Give the position of every Plasmodium parasite.
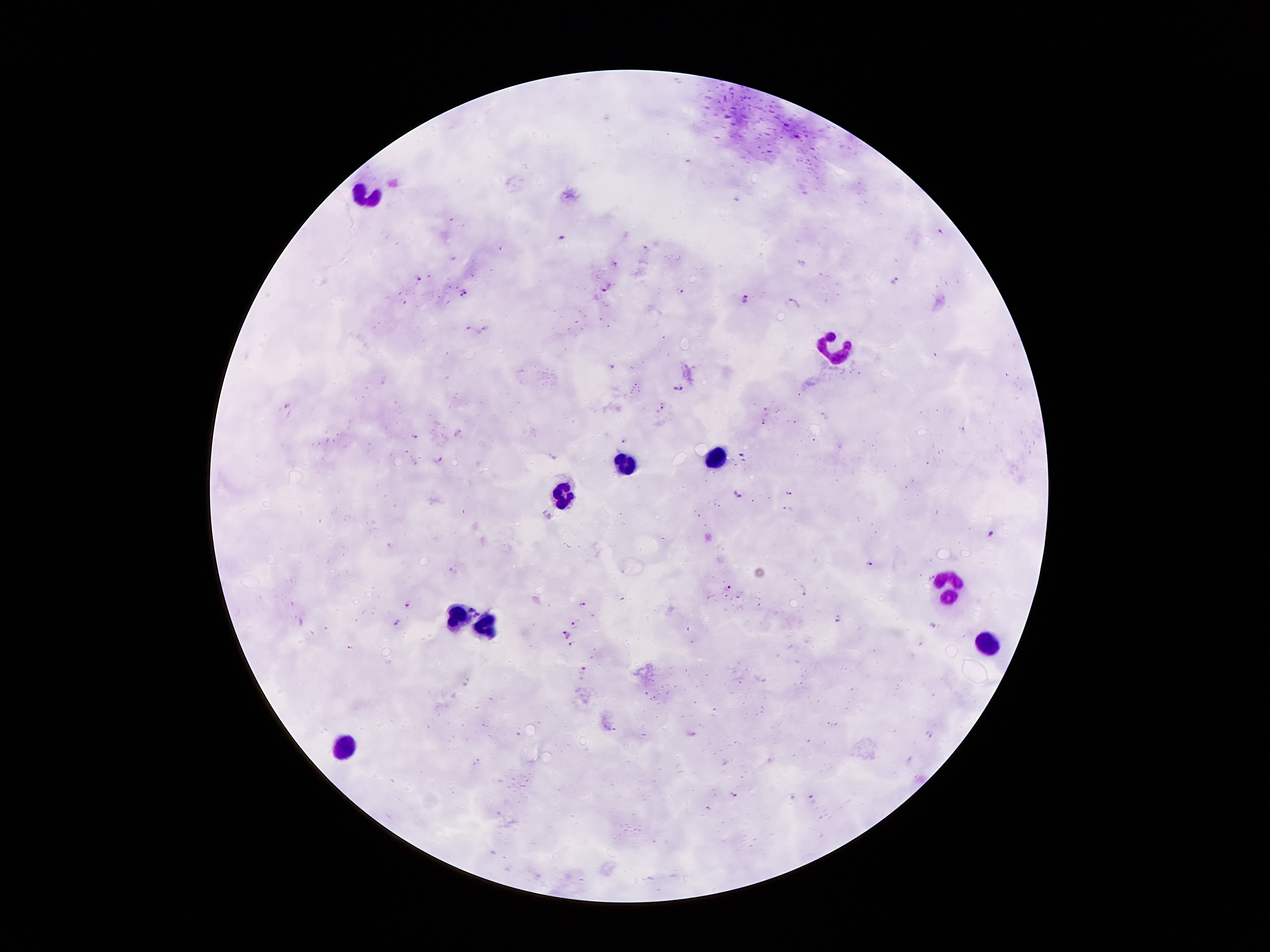
Approximate centers as [x, y] in pixels.
Plasmodium parasites: [940, 232], [562, 237], [615, 262], [419, 278], [897, 282], [609, 288], [465, 292], [680, 292], [747, 297], [794, 302], [484, 330], [613, 365], [678, 388], [288, 404], [662, 407], [793, 421], [762, 422], [962, 429], [458, 433], [414, 438], [624, 439], [439, 459], [790, 493], [738, 495], [992, 533], [870, 563], [453, 570], [729, 588], [804, 592], [582, 603], [408, 605], [837, 618], [399, 622], [575, 625], [933, 625], [566, 635], [571, 643], [584, 668], [930, 734], [735, 793], [812, 799].

Summary:
  - Leukocyte locations: [363, 192], [832, 346], [715, 458], [626, 462], [562, 494], [949, 588], [458, 616], [488, 628], [987, 642], [345, 744]
  - Field of view: single
  - Stain: Giemsa
  - Magnification: 100x
  - Image size: 1270×952 pixels
  - Patient malaria status: positive for Plasmodium falciparum
  - Capture: smartphone through the microscope eyepiece
  - Preparation: thick blood smear